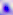 Captured at 400x magnification. Photomicrograph. Toxoplasma gondii is shown.